State which cell type is depicted.
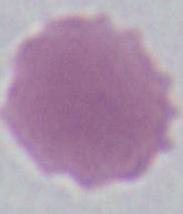
This is an erythrocyte.

{
  "modality": "micrograph",
  "magnification": "1000x"
}